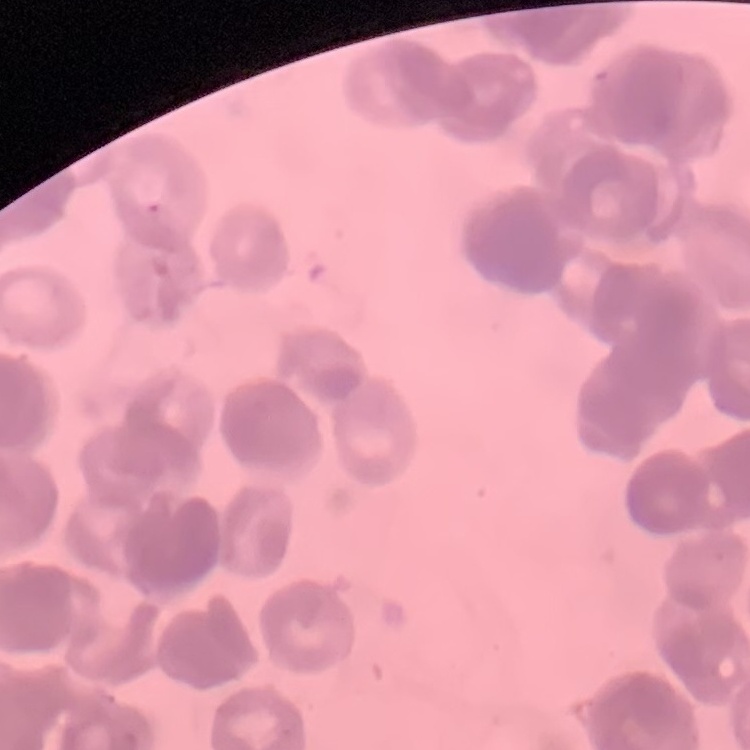

The erythrocytes exhibit rouleaux formation. One tile cut from a larger photomicrograph. Stained with either Field's or Giemsa. Thin blood film.